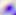

magnification = 400x
identification = Toxoplasma gondii
modality = photomicrograph